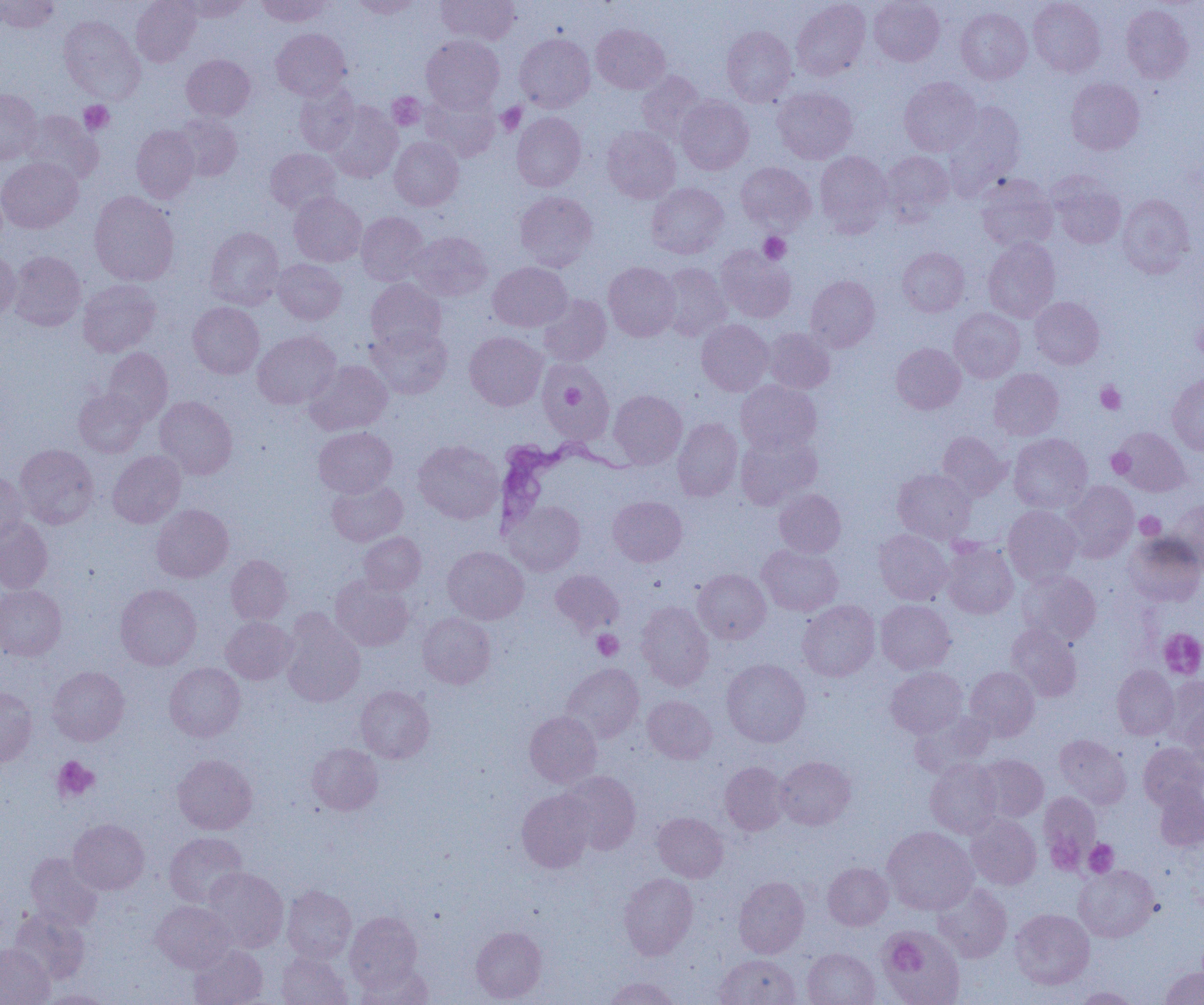

trypanosoma_brucei_locations: 'approximate bounding boxes as named x1/y1/x2/y2 corners in pixels: (x1=492, y1=434, x2=641, y2=538)'
slide_level_diagnosis: Trypanosoma brucei
magnification: 1000x
preparation: thin blood smear
image_size: 1204×1005 pixels
platelet_locations: 'approximate bounding boxes as named x1/y1/x2/y2 corners in pixels: (x1=387, y1=93, x2=425, y2=130), (x1=79, y1=101, x2=114, y2=134), (x1=496, y1=102, x2=526, y2=135), (x1=759, y1=232, x2=791, y2=264), (x1=1193, y1=319, x2=1204, y2=361), (x1=556, y1=375, x2=592, y2=422), (x1=1096, y1=381, x2=1126, y2=414), (x1=1107, y1=448, x2=1135, y2=478), (x1=1135, y1=512, x2=1165, y2=539), (x1=1158, y1=628, x2=1204, y2=679), (x1=592, y1=630, x2=623, y2=660), (x1=53, y1=756, x2=99, y2=801), (x1=1045, y1=837, x2=1085, y2=875), (x1=1084, y1=839, x2=1118, y2=877), (x1=887, y1=938, x2=924, y2=972)'
uninfected_red_blood_cell_locations: 'approximate bounding boxes as named x1/y1/x2/y2 corners in pixels: (x1=0, y1=0, x2=59, y2=33), (x1=131, y1=0, x2=201, y2=66), (x1=178, y1=0, x2=252, y2=21), (x1=257, y1=0, x2=330, y2=26), (x1=349, y1=0, x2=422, y2=18), (x1=436, y1=0, x2=519, y2=45), (x1=792, y1=0, x2=870, y2=81), (x1=869, y1=0, x2=944, y2=66), (x1=1028, y1=0, x2=1105, y2=77), (x1=1121, y1=4, x2=1194, y2=84), (x1=956, y1=7, x2=1032, y2=84), (x1=59, y1=16, x2=144, y2=103), (x1=591, y1=24, x2=670, y2=94), (x1=722, y1=26, x2=797, y2=106), (x1=271, y1=28, x2=351, y2=100), (x1=515, y1=33, x2=594, y2=112), (x1=422, y1=35, x2=504, y2=112), (x1=182, y1=54, x2=255, y2=121), (x1=636, y1=71, x2=706, y2=143), (x1=900, y1=77, x2=982, y2=156), (x1=1066, y1=78, x2=1145, y2=154), (x1=294, y1=83, x2=359, y2=154), (x1=773, y1=87, x2=857, y2=164), (x1=0, y1=88, x2=41, y2=163), (x1=421, y1=91, x2=500, y2=161), (x1=676, y1=96, x2=753, y2=174), (x1=323, y1=102, x2=402, y2=182), (x1=945, y1=102, x2=1025, y2=189), (x1=21, y1=110, x2=103, y2=185), (x1=512, y1=112, x2=586, y2=191), (x1=174, y1=114, x2=243, y2=181), (x1=131, y1=125, x2=199, y2=202), (x1=602, y1=126, x2=681, y2=203), (x1=389, y1=137, x2=463, y2=210), (x1=265, y1=148, x2=341, y2=214), (x1=814, y1=151, x2=892, y2=234), (x1=880, y1=151, x2=954, y2=223), (x1=0, y1=156, x2=83, y2=233), (x1=736, y1=162, x2=816, y2=233), (x1=977, y1=174, x2=1058, y2=251), (x1=1048, y1=174, x2=1126, y2=249), (x1=646, y1=183, x2=729, y2=258), (x1=89, y1=191, x2=179, y2=286), (x1=514, y1=191, x2=597, y2=271), (x1=289, y1=192, x2=366, y2=267), (x1=1117, y1=194, x2=1195, y2=278), (x1=356, y1=211, x2=428, y2=285), (x1=205, y1=227, x2=284, y2=309), (x1=408, y1=231, x2=492, y2=301), (x1=983, y1=238, x2=1060, y2=323), (x1=716, y1=246, x2=796, y2=323), (x1=897, y1=247, x2=969, y2=317), (x1=0, y1=249, x2=20, y2=322), (x1=8, y1=251, x2=86, y2=331), (x1=273, y1=259, x2=346, y2=324), (x1=488, y1=262, x2=571, y2=331), (x1=603, y1=262, x2=680, y2=341), (x1=659, y1=262, x2=730, y2=341), (x1=806, y1=275, x2=880, y2=351), (x1=366, y1=279, x2=446, y2=353), (x1=78, y1=280, x2=160, y2=356), (x1=538, y1=294, x2=611, y2=365), (x1=1030, y1=297, x2=1104, y2=369), (x1=188, y1=302, x2=264, y2=378), (x1=949, y1=308, x2=1024, y2=383), (x1=697, y1=320, x2=773, y2=395), (x1=368, y1=325, x2=452, y2=399), (x1=763, y1=328, x2=835, y2=393), (x1=252, y1=331, x2=340, y2=409), (x1=464, y1=332, x2=547, y2=410), (x1=891, y1=343, x2=965, y2=414), (x1=102, y1=348, x2=172, y2=425), (x1=306, y1=360, x2=392, y2=435), (x1=539, y1=362, x2=614, y2=442), (x1=989, y1=368, x2=1064, y2=440), (x1=1168, y1=373, x2=1204, y2=454), (x1=736, y1=381, x2=821, y2=453), (x1=74, y1=388, x2=147, y2=457), (x1=609, y1=390, x2=687, y2=468), (x1=155, y1=396, x2=237, y2=479), (x1=673, y1=418, x2=742, y2=501), (x1=314, y1=426, x2=397, y2=497), (x1=1110, y1=426, x2=1192, y2=497), (x1=735, y1=430, x2=821, y2=509), (x1=937, y1=431, x2=1009, y2=499), (x1=1009, y1=433, x2=1092, y2=513), (x1=413, y1=440, x2=503, y2=524), (x1=15, y1=444, x2=98, y2=529), (x1=108, y1=451, x2=186, y2=528), (x1=893, y1=468, x2=976, y2=543), (x1=0, y1=470, x2=28, y2=544), (x1=327, y1=480, x2=407, y2=546), (x1=1062, y1=481, x2=1138, y2=563), (x1=774, y1=488, x2=846, y2=557), (x1=608, y1=496, x2=687, y2=566), (x1=1166, y1=499, x2=1204, y2=569), (x1=504, y1=501, x2=585, y2=575), (x1=151, y1=504, x2=233, y2=582), (x1=1003, y1=506, x2=1081, y2=585), (x1=0, y1=517, x2=53, y2=594), (x1=874, y1=529, x2=952, y2=605), (x1=358, y1=532, x2=426, y2=595), (x1=1124, y1=533, x2=1204, y2=606), (x1=941, y1=540, x2=1018, y2=618), (x1=757, y1=545, x2=842, y2=615), (x1=443, y1=546, x2=529, y2=624), (x1=227, y1=555, x2=292, y2=624), (x1=550, y1=569, x2=624, y2=635), (x1=693, y1=569, x2=770, y2=643), (x1=1018, y1=570, x2=1101, y2=645), (x1=331, y1=576, x2=413, y2=651), (x1=115, y1=584, x2=201, y2=670), (x1=0, y1=585, x2=66, y2=660), (x1=797, y1=600, x2=880, y2=681), (x1=876, y1=600, x2=955, y2=674), (x1=636, y1=602, x2=714, y2=690), (x1=281, y1=613, x2=365, y2=707), (x1=418, y1=613, x2=496, y2=688), (x1=221, y1=616, x2=296, y2=684), (x1=1006, y1=624, x2=1082, y2=701), (x1=721, y1=659, x2=810, y2=747), (x1=164, y1=663, x2=245, y2=741), (x1=561, y1=663, x2=644, y2=742), (x1=1112, y1=665, x2=1178, y2=739), (x1=48, y1=666, x2=129, y2=745), (x1=886, y1=667, x2=967, y2=738), (x1=965, y1=667, x2=1039, y2=741), (x1=1160, y1=676, x2=1204, y2=747), (x1=356, y1=685, x2=434, y2=763), (x1=0, y1=687, x2=37, y2=766), (x1=643, y1=695, x2=717, y2=763), (x1=1184, y1=706, x2=1204, y2=774), (x1=910, y1=710, x2=994, y2=777), (x1=525, y1=711, x2=602, y2=787), (x1=1054, y1=734, x2=1131, y2=808), (x1=1138, y1=742, x2=1204, y2=809), (x1=307, y1=743, x2=383, y2=814), (x1=173, y1=754, x2=257, y2=834), (x1=974, y1=754, x2=1048, y2=822), (x1=775, y1=756, x2=855, y2=829), (x1=925, y1=759, x2=1003, y2=838), (x1=720, y1=761, x2=789, y2=835), (x1=559, y1=770, x2=641, y2=853), (x1=1153, y1=785, x2=1204, y2=851), (x1=517, y1=790, x2=595, y2=872), (x1=1039, y1=791, x2=1100, y2=866), (x1=653, y1=812, x2=728, y2=882), (x1=966, y1=814, x2=1041, y2=889), (x1=68, y1=818, x2=150, y2=894), (x1=882, y1=826, x2=977, y2=914), (x1=164, y1=832, x2=248, y2=907), (x1=25, y1=852, x2=103, y2=930), (x1=823, y1=862, x2=893, y2=930), (x1=1075, y1=865, x2=1159, y2=941), (x1=203, y1=867, x2=288, y2=952), (x1=619, y1=873, x2=698, y2=959), (x1=734, y1=876, x2=809, y2=958), (x1=933, y1=883, x2=1012, y2=962), (x1=282, y1=885, x2=356, y2=963), (x1=151, y1=901, x2=236, y2=972), (x1=1010, y1=908, x2=1094, y2=989), (x1=10, y1=909, x2=90, y2=984), (x1=345, y1=911, x2=422, y2=992), (x1=880, y1=925, x2=965, y2=1005), (x1=471, y1=926, x2=546, y2=1002), (x1=0, y1=944, x2=54, y2=1005), (x1=188, y1=944, x2=268, y2=1005), (x1=802, y1=948, x2=879, y2=1005), (x1=277, y1=951, x2=352, y2=1005), (x1=715, y1=954, x2=801, y2=1005), (x1=355, y1=964, x2=433, y2=1005), (x1=1159, y1=966, x2=1204, y2=1005), (x1=604, y1=977, x2=680, y2=1004), (x1=1074, y1=987, x2=1141, y2=1004), (x1=41, y1=990, x2=113, y2=1004)'
modality: optical microscopy
field_of_view: single